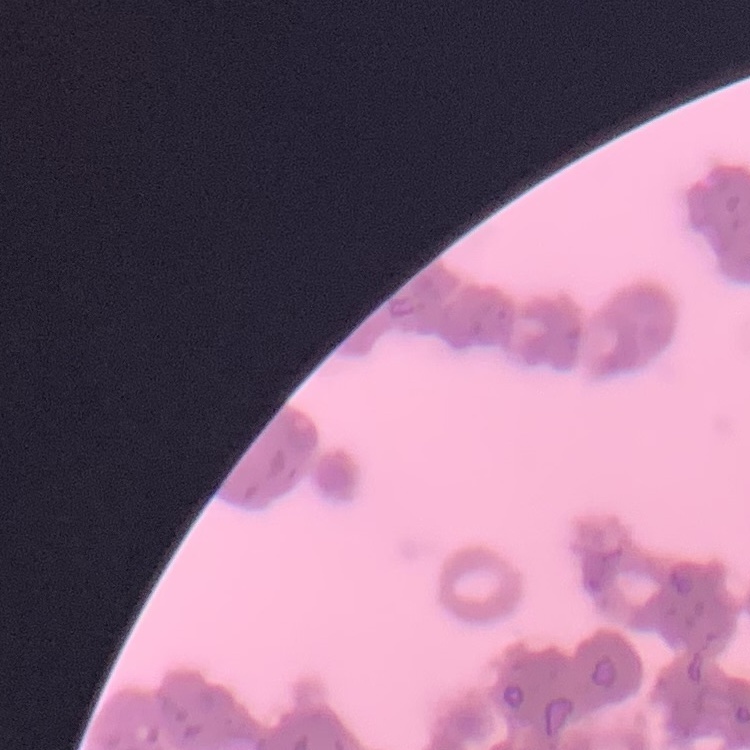
Summary:
  - Red blood cell morphology: rouleaux formation
  - Preparation: thin peripheral smear
  - Stain: Field's or Giemsa
  - Image type: one tile cut from a larger photomicrograph